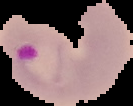

Summary:
  - Image size: 133×106 pixels
  - Image type: segmented cell region with the area outside set to black
  - Malaria status: parasitized
  - Preparation: thin blood film